Report the malaria status of this cell.
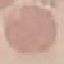

It is uninfected.

capture = smartphone camera at the microscope eyepiece
stain = Giemsa
image type = cell patch, automatically extracted from a larger field of view and resized to 64 × 64 pixels
preparation = thin blood film